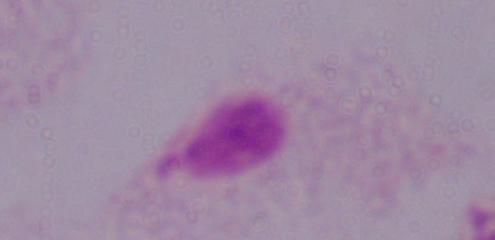
1000x magnification. A trichomonad is seen. Photomicrograph.